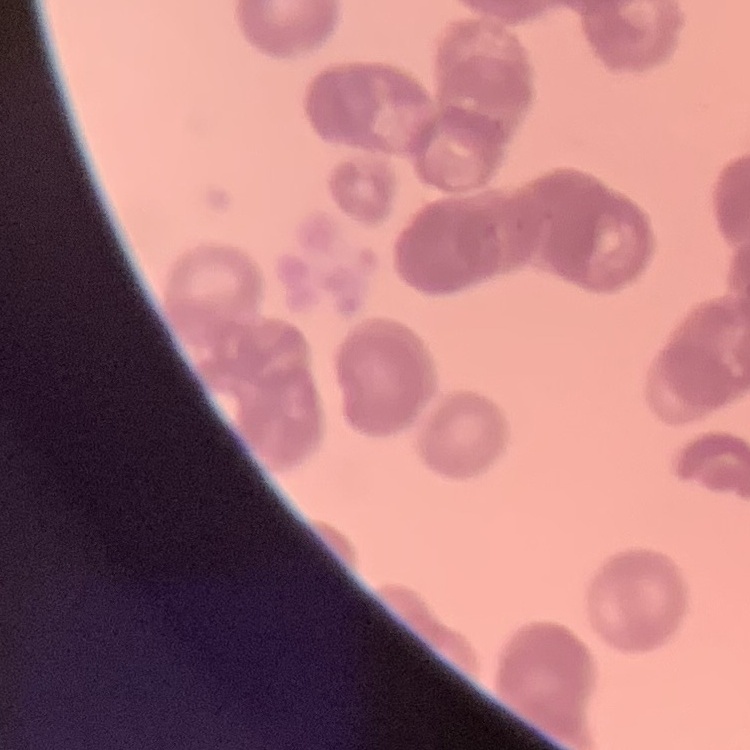

red blood cell morphology = rouleaux formation
image type = square crop of a larger photomicrograph
preparation = thin peripheral smear
stain = Field's or Giemsa